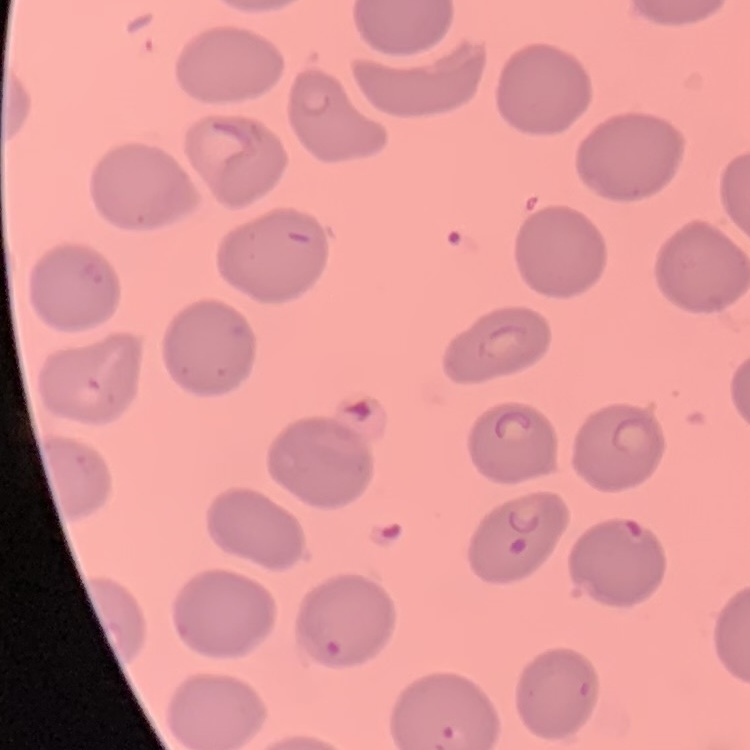
Summary:
  - Red blood cell morphology: no rouleaux formation
  - Stain: Field's or Giemsa
  - Preparation: thin peripheral smear
  - Image type: one tile cut from a larger photomicrograph